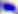

Toxoplasma gondii is shown. Captured at 400x magnification. Photomicrograph.